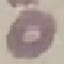

Result: no malaria parasites seen. Acquired by smartphone through the microscope eyepiece. Automatically extracted cell patch, resized to 64 × 64 pixels. Thin smear of blood. Giemsa-stained preparation.